Comment on the morphology of the erythrocytes.
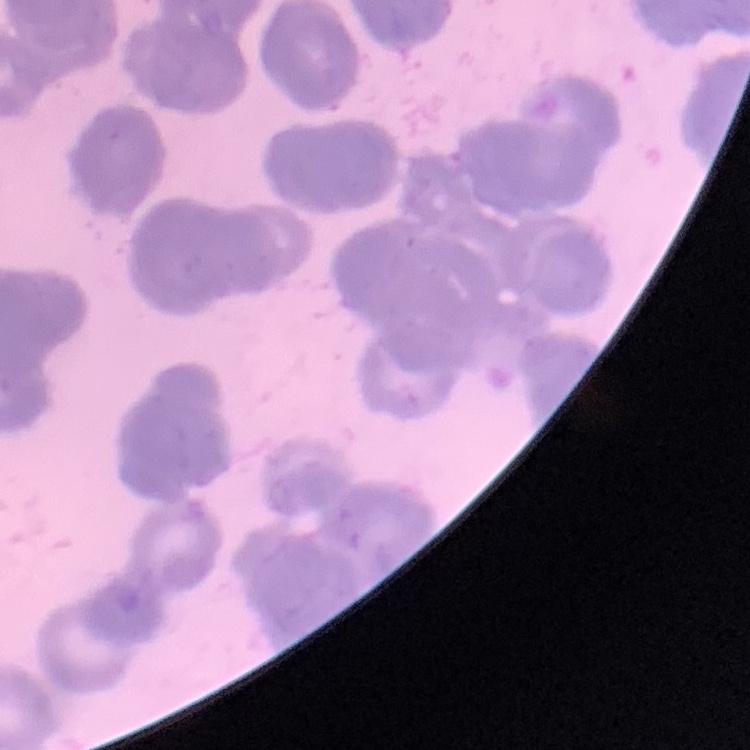
They show rouleaux formation.

Square crop of a larger photomicrograph. Thin blood film. Stained with either Field's or Giemsa.